Identify the parasite.
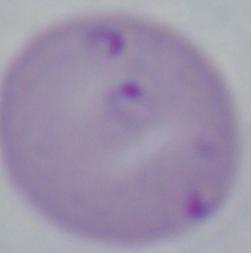
Babesia.

Summary:
  - Magnification: 1000x
  - Modality: photomicrograph